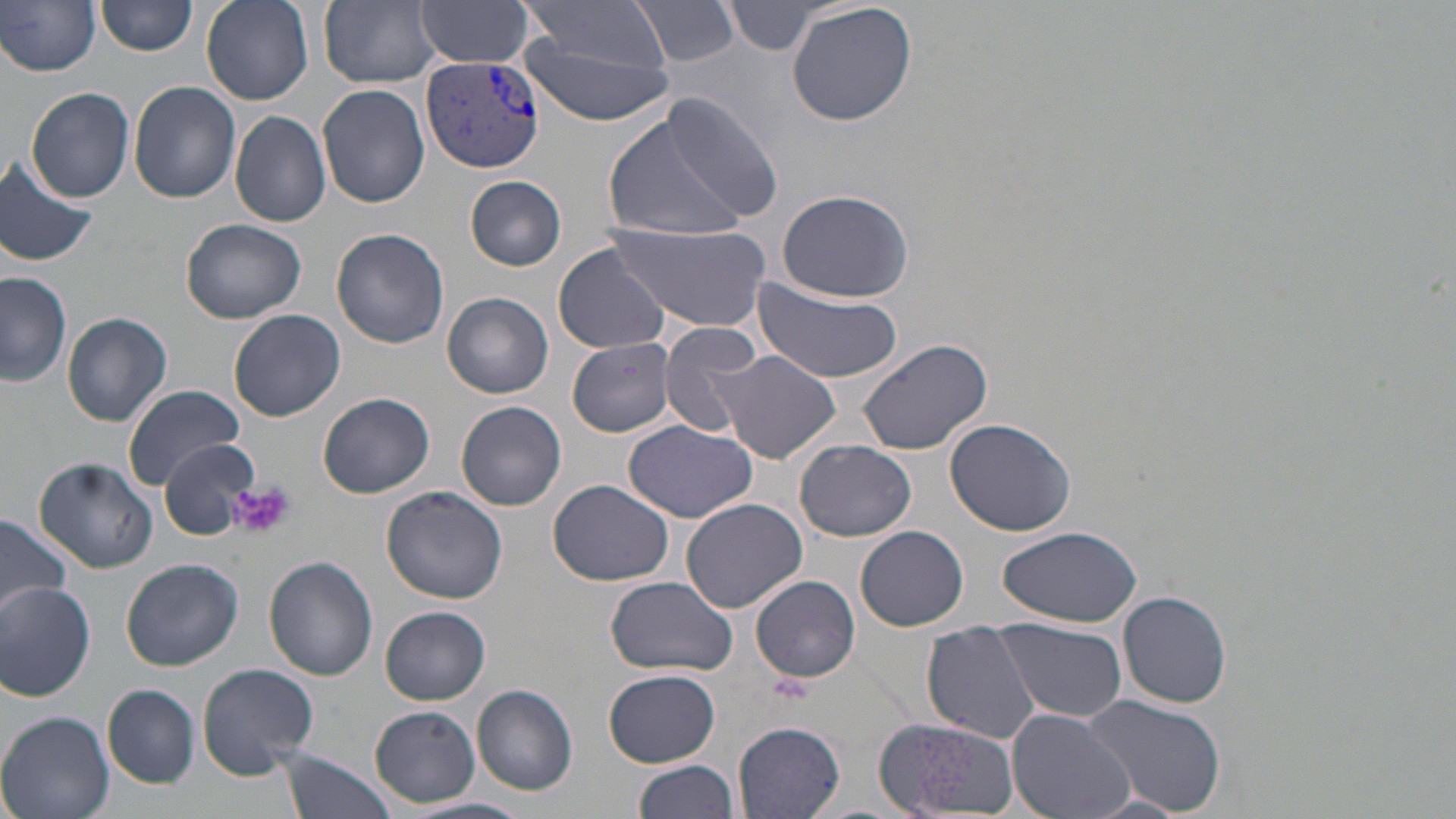
slide-level diagnosis = Plasmodium vivax
magnification = 1000x
platelet locations = approximate bounding boxes as (x1,y1)-(x2,y2) corner pairs in pixels: (229,480)-(294,541)
stain = May-Grünwald-Giemsa
image size = 1456×819 pixels
Plasmodium vivax-infected red blood cell locations = approximate bounding boxes as (x1,y1)-(x2,y2) corner pairs in pixels: (418,57)-(547,172)
field of view = single
preparation = thin blood film
modality = optical microscopy
uninfected red blood cell locations = approximate bounding boxes as (x1,y1)-(x2,y2) corner pairs in pixels: (200,0)-(314,106), (318,0)-(442,88), (629,0)-(743,67), (1,1)-(102,75), (97,1)-(199,57), (414,1)-(536,69), (519,1)-(670,72), (786,2)-(916,126), (724,3)-(829,54), (517,33)-(673,126), (129,82)-(242,203), (318,83)-(431,208), (26,86)-(135,202), (660,96)-(786,223), (601,109)-(755,245), (230,110)-(331,228), (0,156)-(99,268), (465,175)-(567,270), (775,189)-(915,302), (182,218)-(307,324), (607,220)-(773,334), (331,228)-(450,349), (552,243)-(670,356), (0,271)-(73,388), (750,278)-(905,383), (443,292)-(554,398), (229,309)-(345,422), (62,310)-(172,426), (657,323)-(767,436), (856,337)-(993,457), (567,338)-(675,437), (715,351)-(842,463), (121,383)-(243,487), (318,392)-(435,496), (456,401)-(567,511), (944,417)-(1077,535), (623,420)-(759,523), (160,438)-(259,541), (795,439)-(917,541), (34,458)-(159,572), (549,477)-(674,586), (380,486)-(508,604), (681,498)-(807,612), (0,513)-(72,619), (856,525)-(968,631), (998,525)-(1142,628), (264,556)-(379,681), (122,558)-(242,670), (751,575)-(860,682), (604,576)-(736,676), (0,581)-(97,700), (1118,591)-(1232,708), (380,606)-(490,704), (997,620)-(1128,721), (922,621)-(1042,745), (196,663)-(319,775), (603,670)-(721,767), (103,685)-(201,786), (472,686)-(577,794), (1082,693)-(1226,817), (369,707)-(479,806), (1007,709)-(1136,819), (0,712)-(116,819), (733,719)-(846,818), (871,719)-(1022,816), (276,749)-(398,819), (634,759)-(740,819), (403,797)-(532,819)